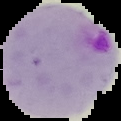
Summary:
  - Preparation: thin blood film
  - Malaria status: parasitized
  - Image size: 121×121 pixels
  - Image type: segmented cell region with the area outside set to black